Name the parasite shown.
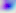

Toxoplasma gondii.

Summary:
  - Modality: micrograph
  - Magnification: 400x